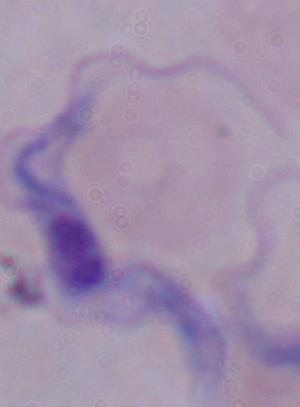 Photomicrograph. A trypanosome is shown. Captured at 1000x magnification.